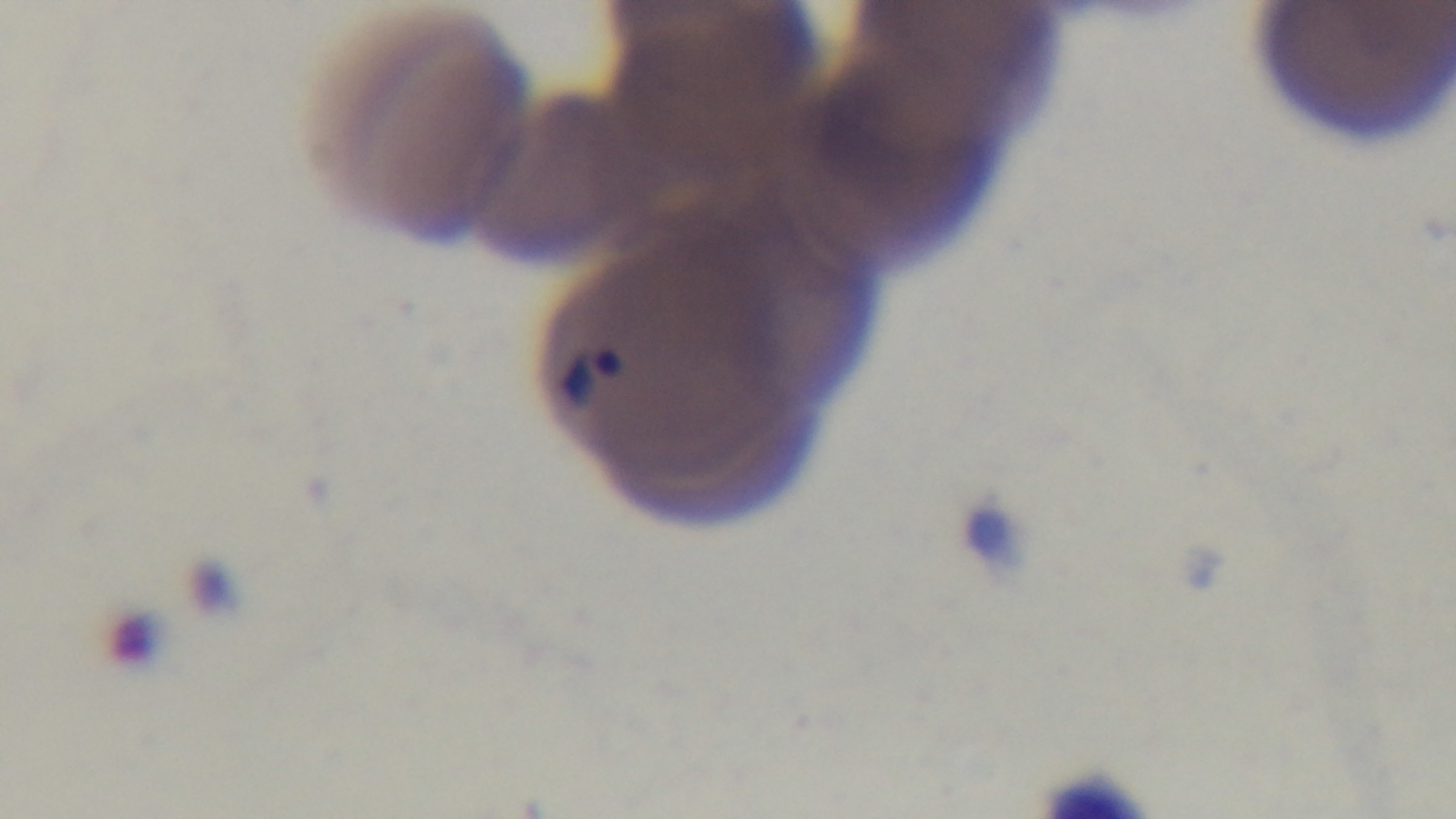

preparation = thin smear
capture = mounted 4K digital camera
modality = light microscopy
objective = 100x oil immersion
field of view = single
malaria status = infected
stain = Giemsa